State the preparation type.
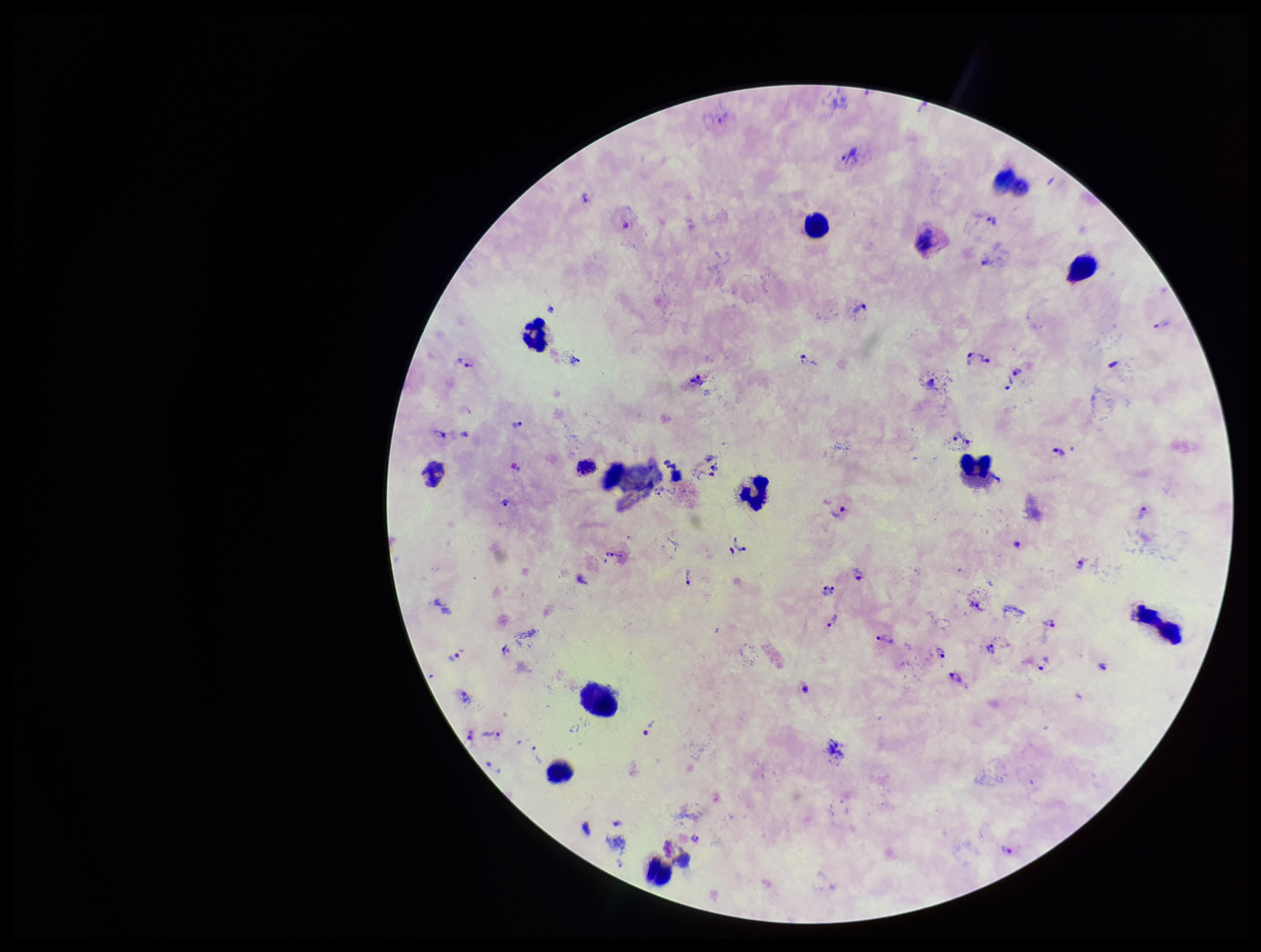
It is a thick blood smear.

Stained with Giemsa. Photographed through the microscope eyepiece with a smartphone camera. Leukocyte count: 12. Plasmodium parasites: seen. Patient malaria status: infected. Image is 1261×952 pixels. Parasite count: 46. Single field of view. Species reported for this patient: Plasmodium vivax.